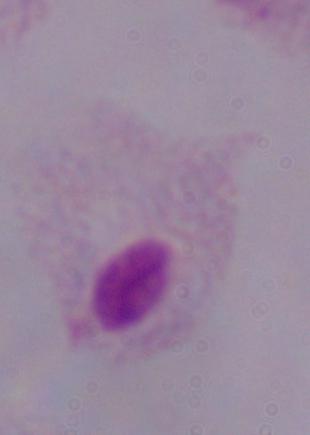 Photomicrograph. A trichomonad is seen. 1000x magnification.